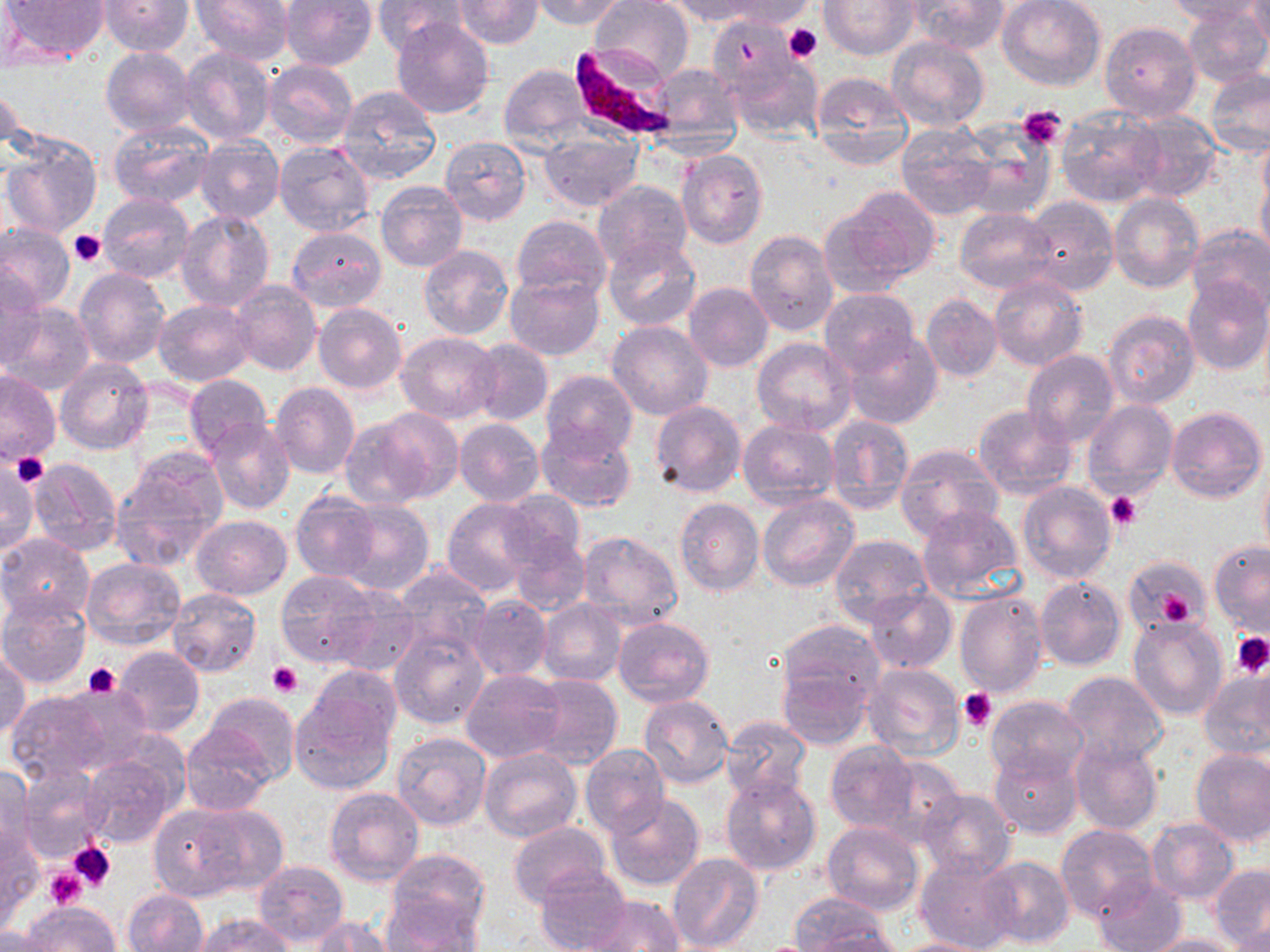
{
  "slide_level_diagnosis": "Plasmodium falciparum",
  "magnification": "1000x",
  "modality": "optical microscopy",
  "uninfected_red_blood_cell_locations": "approximate bounding boxes as [x1, y1, x2, y2] in pixels: [6, 0, 107, 62], [101, 0, 193, 55], [190, 0, 293, 66], [280, 0, 377, 71], [373, 0, 467, 56], [453, 0, 545, 47], [529, 0, 628, 28], [590, 0, 694, 84], [711, 0, 813, 29], [820, 0, 918, 59], [910, 0, 1007, 53], [998, 0, 1106, 90], [1164, 0, 1270, 25], [1242, 0, 1270, 49], [668, 1, 770, 26], [1181, 2, 1269, 88], [708, 13, 800, 104], [390, 17, 494, 118], [1099, 21, 1200, 121], [886, 37, 989, 131], [100, 47, 197, 137], [181, 47, 277, 147], [727, 50, 823, 142], [263, 59, 358, 147], [649, 63, 743, 144], [499, 64, 592, 154], [1206, 70, 1270, 158], [810, 72, 913, 168], [1, 82, 23, 162], [336, 85, 443, 185], [1055, 106, 1163, 209], [1124, 108, 1222, 202], [109, 120, 215, 208], [895, 123, 996, 220], [957, 123, 1053, 222], [538, 128, 641, 213], [1257, 133, 1270, 224], [1, 136, 101, 239], [195, 136, 285, 223], [440, 136, 531, 224], [273, 139, 374, 235], [676, 149, 767, 249], [1256, 171, 1269, 265], [593, 180, 691, 272], [376, 182, 467, 273], [836, 184, 940, 285], [1109, 192, 1203, 293], [97, 193, 194, 283], [1023, 195, 1118, 295], [955, 207, 1057, 293], [176, 208, 275, 312], [511, 214, 612, 302], [0, 223, 75, 312], [1185, 224, 1270, 315], [287, 227, 386, 311], [744, 229, 839, 336], [604, 237, 701, 331], [418, 246, 513, 339], [73, 268, 171, 370], [1, 269, 45, 368], [505, 273, 605, 361], [988, 275, 1087, 372], [1183, 277, 1270, 376], [230, 280, 321, 376], [683, 282, 773, 372], [819, 289, 918, 378], [921, 294, 1003, 382], [154, 299, 253, 386], [5, 302, 95, 395], [312, 304, 407, 394], [1102, 309, 1200, 408], [608, 320, 714, 420], [842, 329, 944, 428], [395, 331, 501, 423], [469, 339, 552, 425], [752, 339, 856, 436], [1022, 351, 1119, 448], [473, 355, 632, 442], [55, 358, 153, 454], [541, 369, 638, 457], [0, 370, 61, 465], [184, 373, 272, 457], [271, 382, 360, 479], [1083, 400, 1178, 501], [650, 401, 745, 497], [972, 404, 1079, 498], [1166, 405, 1266, 503], [361, 408, 464, 505], [825, 415, 915, 513], [205, 417, 295, 515], [454, 418, 544, 507], [739, 419, 838, 510], [537, 421, 636, 513], [894, 444, 1003, 541], [110, 453, 225, 570], [0, 457, 40, 558], [27, 458, 122, 555], [1258, 466, 1270, 561], [1017, 482, 1117, 585], [498, 491, 585, 568], [291, 492, 381, 584], [757, 493, 860, 591], [334, 498, 434, 595], [442, 498, 539, 595], [673, 498, 765, 595], [916, 505, 1024, 603], [192, 515, 292, 600], [576, 530, 683, 633], [0, 533, 94, 626], [509, 533, 590, 616], [829, 533, 932, 625], [1209, 541, 1270, 638], [1124, 556, 1210, 636], [79, 557, 187, 650], [391, 563, 492, 658], [276, 569, 382, 667], [1035, 576, 1126, 671], [325, 585, 423, 678], [865, 587, 957, 673], [167, 588, 261, 677], [955, 588, 1050, 698], [469, 595, 552, 681], [0, 596, 90, 688], [538, 599, 625, 687], [1129, 616, 1228, 721], [612, 617, 714, 708], [776, 620, 884, 713], [390, 629, 489, 729], [112, 645, 204, 738], [0, 649, 30, 741], [863, 660, 965, 760], [307, 664, 402, 748], [776, 664, 872, 750], [462, 670, 565, 762], [1200, 670, 1270, 762], [1060, 671, 1169, 765], [525, 673, 622, 769], [289, 680, 397, 795], [6, 686, 127, 783], [201, 691, 300, 786], [985, 694, 1089, 784], [638, 695, 734, 789], [721, 716, 811, 802], [182, 723, 275, 815], [390, 731, 490, 832], [1071, 738, 1163, 835], [825, 742, 916, 832], [580, 746, 671, 838], [988, 747, 1083, 837], [480, 749, 582, 843], [1190, 749, 1270, 847], [866, 753, 968, 845], [83, 756, 176, 848], [0, 763, 36, 860], [15, 766, 110, 861], [720, 773, 822, 875], [325, 787, 424, 884], [918, 789, 1016, 880], [604, 792, 705, 892], [152, 801, 274, 901], [1147, 819, 1239, 903], [822, 821, 924, 916], [508, 822, 612, 909], [1056, 825, 1158, 924], [0, 828, 43, 929], [386, 848, 490, 942], [915, 851, 1023, 952], [668, 852, 764, 952], [980, 855, 1073, 948], [254, 860, 349, 946], [534, 864, 632, 952], [1210, 864, 1270, 950], [1092, 877, 1188, 952], [122, 888, 208, 952], [384, 894, 484, 950], [577, 895, 685, 951], [787, 895, 899, 951], [19, 903, 120, 952], [193, 914, 298, 952], [305, 916, 398, 951], [0, 926, 57, 952], [1141, 933, 1245, 952], [886, 937, 997, 952]",
  "platelet_locations": "approximate bounding boxes as [x1, y1, x2, y2] in pixels: [783, 23, 823, 62], [1018, 104, 1067, 150], [69, 231, 108, 265], [13, 454, 48, 485], [1106, 491, 1141, 530], [1143, 574, 1200, 628], [1231, 632, 1270, 677], [269, 661, 302, 698], [83, 662, 120, 697], [958, 689, 997, 730], [67, 840, 116, 893], [45, 870, 85, 909]",
  "plasmodium_falciparum_infected_red_blood_cell_locations": "approximate bounding boxes as [x1, y1, x2, y2] in pixels: [568, 46, 681, 142]",
  "field_of_view": "single",
  "preparation": "thin blood smear",
  "stain": "May-Grünwald-Giemsa",
  "image_size": "1270×952 pixels"
}